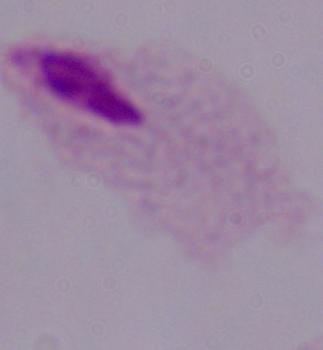
A trichomonad is seen. Photomicrograph. Captured at 1000x magnification.